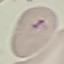

malaria_status: uninfected
image_type: automatically extracted cell patch, resized to 64 × 64 pixels
capture: smartphone through the microscope eyepiece
stain: Giemsa
preparation: thin blood smear